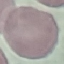

result = negative for malaria parasites
preparation = thin blood film
stain = Giemsa
capture = smartphone camera at the microscope eyepiece
image type = automatically extracted cell patch, resized to 64 × 64 pixels